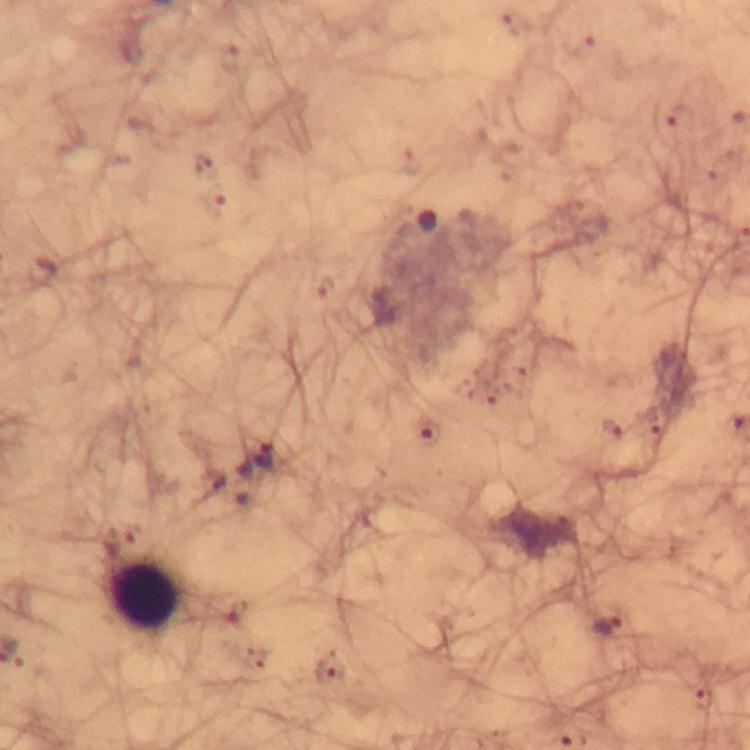
Approximate centers as [x, y] in pixels.
Summary:
  - Malaria parasite locations: [481, 393], [651, 419], [610, 427], [425, 434], [264, 456], [238, 612], [607, 625], [330, 674], [705, 700]
  - Leukocyte locations: [143, 595]
  - Cropped from: a single field of view
  - Image size: 750×750 pixels
  - Capture: smartphone photograph through a microscope
  - Context: from a diagnostic examination for malaria
  - Stain: Giemsa
  - Preparation: thick smear
  - Magnification: 100x
  - Immersion oil: used